Report the malaria status of this cell.
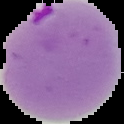
It is parasitized.

From a thin blood film. Cell region segmented out of the field of view; the surrounding area is masked to black. Image is 124×124 pixels.